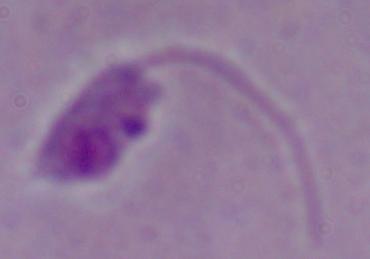
modality = micrograph
identification = Leishmania
magnification = 1000x